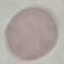

Malaria status: uninfected. Thin smear of blood. Giemsa-stained preparation. Acquired by smartphone through the microscope eyepiece. Cell patch, automatically extracted from a larger field of view and resized to 64 × 64 pixels.